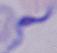

Summary:
  - Magnification: 1000x
  - Identification: trypanosome
  - Modality: photomicrograph